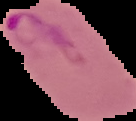
malaria status = parasitized
image type = segmented cell region on a black background
preparation = thin blood smear
image size = 136×121 pixels